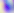
Micrograph. Captured at 400x magnification. Toxoplasma gondii is shown.